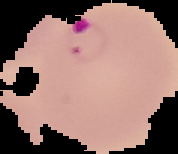

{
  "malaria_status": "parasitized",
  "image_type": "segmented cell region on a black background",
  "image_size": "178×154 pixels",
  "preparation": "thin blood film"
}